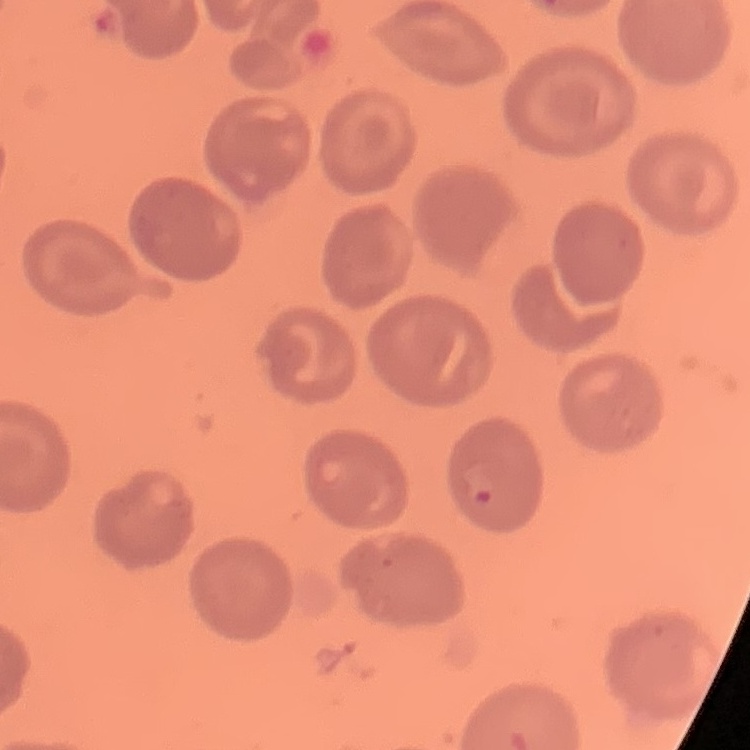

Summary:
  - Red blood cell morphology: no rouleaux formation
  - Stain: Field's or Giemsa
  - Image type: square crop of a larger photomicrograph
  - Preparation: thin peripheral smear